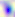
identification = Toxoplasma gondii
modality = micrograph
magnification = 400x